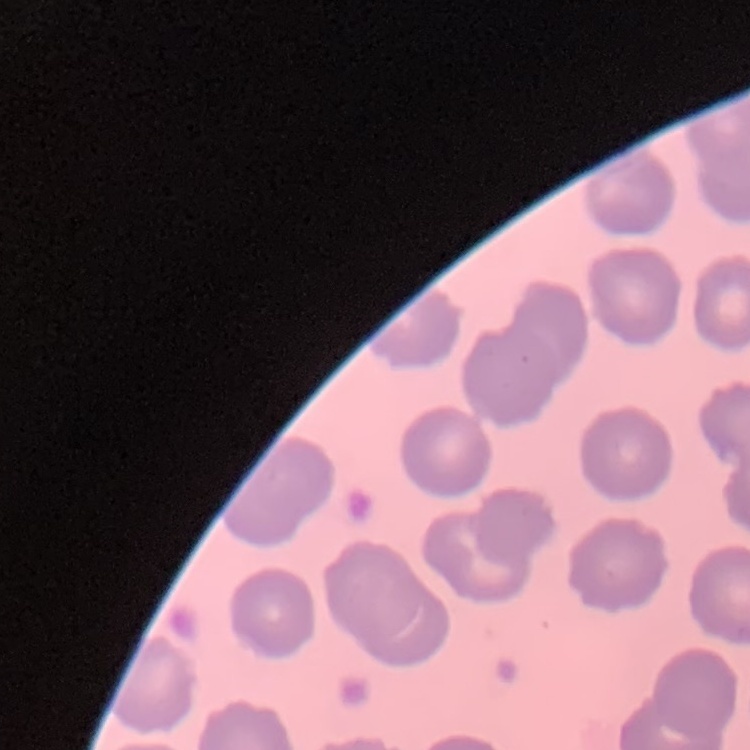
red_blood_cell_morphology: no rouleaux formation
image_type: one tile cut from a larger photomicrograph
preparation: thin blood smear
stain: Field's or Giemsa